Find each parasitized RBC.
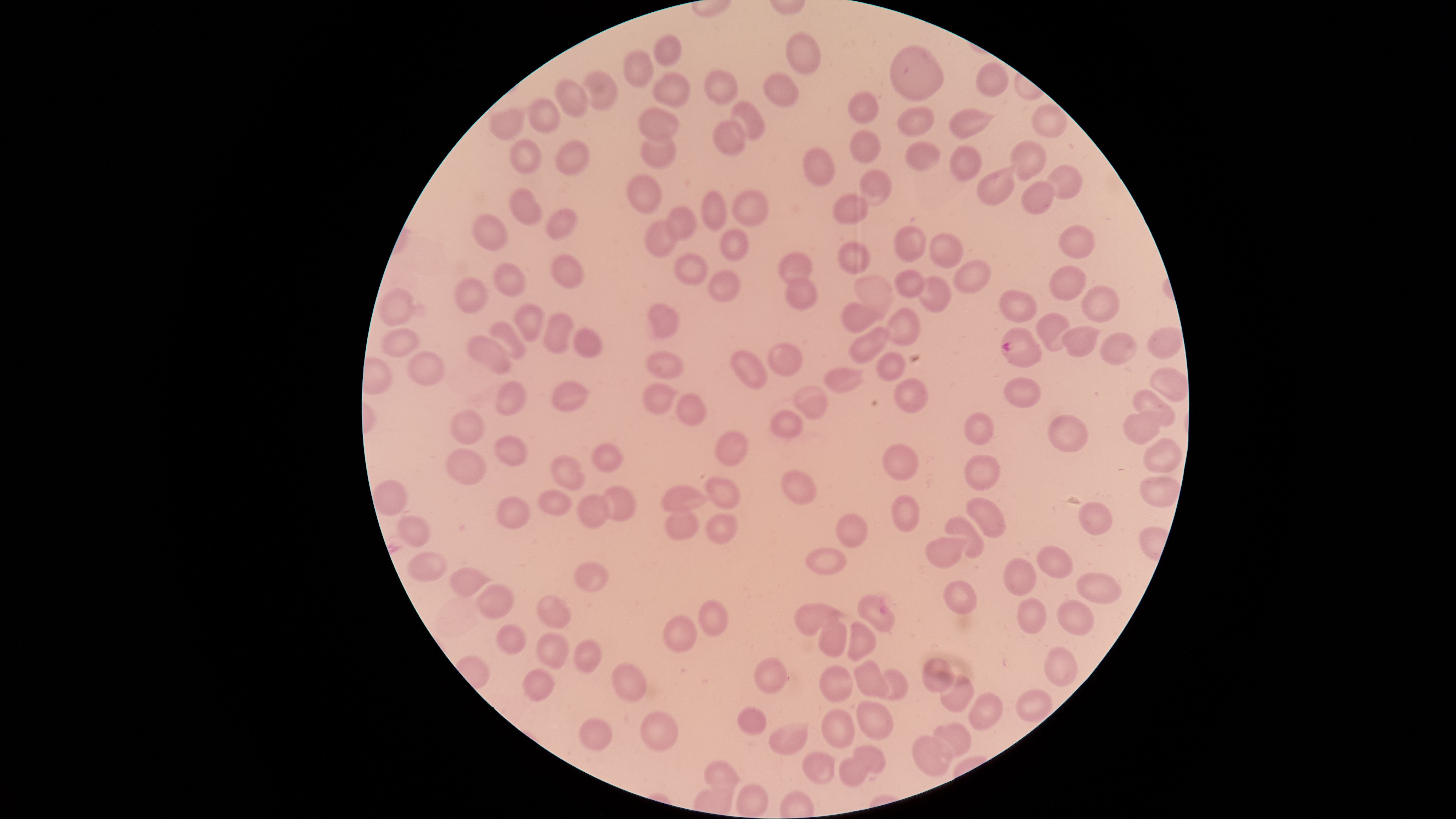

Approximate bounding boxes as (left, top, right, bottom) in pixels.
Parasitized RBCs: (999, 327, 1042, 368).

Approximate bounding boxes as (left, top, right, bottom) in pixels. Uninfected RBCs: (786, 33, 819, 75), (654, 35, 682, 66), (890, 45, 943, 101), (623, 48, 653, 87), (973, 63, 1009, 96), (704, 68, 737, 105), (581, 71, 617, 110), (653, 72, 690, 108), (763, 72, 797, 108), (554, 79, 589, 118), (847, 91, 879, 124), (527, 99, 561, 134), (730, 102, 764, 141), (897, 105, 936, 138), (489, 108, 525, 142), (638, 109, 679, 140), (948, 109, 988, 137), (712, 119, 748, 155), (850, 130, 882, 163), (640, 132, 677, 170), (555, 139, 591, 176), (508, 140, 544, 174), (1009, 140, 1046, 179), (905, 142, 941, 171), (948, 145, 982, 181), (801, 147, 836, 187), (1044, 166, 1083, 199), (859, 169, 894, 207), (975, 169, 1016, 205), (626, 173, 664, 214), (1020, 180, 1057, 215), (509, 187, 543, 226), (733, 190, 769, 226), (703, 192, 727, 230), (831, 194, 869, 225), (666, 206, 697, 239), (545, 210, 580, 240), (472, 213, 509, 253), (644, 219, 678, 258), (1058, 225, 1096, 258), (895, 226, 926, 263), (720, 228, 748, 261), (928, 233, 964, 268), (838, 242, 872, 275), (674, 251, 710, 286), (550, 252, 585, 288), (779, 253, 812, 285), (952, 258, 990, 295), (493, 262, 525, 297), (1049, 264, 1085, 302), (895, 269, 924, 300), (709, 270, 741, 302), (454, 276, 489, 313), (855, 276, 893, 313), (786, 277, 818, 310), (918, 277, 952, 313), (1082, 286, 1118, 323), (377, 289, 417, 325), (999, 290, 1037, 323), (840, 302, 878, 333), (511, 303, 547, 342), (647, 303, 680, 337), (885, 308, 921, 347), (541, 312, 576, 355), (1036, 313, 1073, 351), (489, 321, 527, 360), (1064, 326, 1097, 357), (381, 327, 420, 357), (848, 327, 891, 364), (573, 329, 603, 359), (1101, 333, 1136, 365), (466, 335, 513, 374), (768, 343, 803, 377), (407, 350, 445, 387), (731, 350, 768, 389), (645, 351, 683, 379), (877, 352, 905, 380), (824, 366, 865, 393), (1003, 378, 1041, 408), (496, 379, 527, 415), (894, 380, 929, 412), (551, 382, 587, 411), (643, 383, 673, 415), (794, 385, 828, 419), (1132, 389, 1175, 427), (675, 394, 707, 426), (450, 408, 485, 444), (770, 410, 803, 438), (965, 411, 994, 447), (1122, 413, 1159, 445), (1048, 414, 1088, 453), (716, 429, 750, 467), (493, 436, 527, 465), (1141, 436, 1182, 474), (591, 442, 625, 471), (881, 443, 919, 481), (445, 449, 489, 486), (965, 454, 1000, 490), (551, 455, 586, 489), (781, 469, 816, 505), (704, 475, 741, 508), (1138, 476, 1179, 506), (662, 482, 708, 513), (602, 486, 635, 522), (540, 489, 572, 516), (579, 494, 609, 530), (497, 496, 531, 529), (890, 496, 921, 531), (967, 497, 1006, 538), (1078, 502, 1114, 536), (666, 505, 702, 540), (707, 513, 739, 544), (836, 513, 868, 548), (397, 514, 432, 547), (946, 516, 984, 558), (926, 534, 970, 569), (1037, 545, 1073, 579), (805, 546, 846, 576), (407, 551, 447, 581), (1003, 558, 1037, 597), (576, 562, 609, 592), (451, 567, 492, 598), (1077, 571, 1120, 605), (943, 581, 976, 615), (477, 584, 514, 618), (536, 595, 572, 628), (857, 595, 896, 632), (1017, 597, 1049, 634), (700, 600, 728, 637), (1057, 601, 1093, 636), (795, 603, 839, 635), (664, 615, 697, 654), (816, 617, 850, 659), (839, 622, 875, 660), (497, 624, 526, 654), (537, 631, 569, 667), (574, 638, 602, 673), (1043, 648, 1076, 687), (753, 656, 787, 695), (922, 658, 954, 692), (853, 660, 890, 703), (612, 663, 648, 702), (819, 666, 854, 701), (523, 667, 556, 700), (874, 670, 909, 701), (941, 675, 974, 713), (1016, 689, 1053, 721), (968, 692, 1003, 731), (858, 701, 894, 740), (737, 707, 767, 735), (821, 710, 857, 749), (640, 711, 677, 752), (579, 718, 613, 751), (768, 722, 809, 754), (932, 723, 970, 759), (913, 735, 953, 776), (851, 745, 886, 772), (801, 752, 835, 783), (838, 758, 870, 787), (702, 760, 739, 794). Species: Plasmodium falciparum. Smartphone photograph through the microscope eyepiece. Image is 1456×819 pixels. Giemsa stain. Circular visible region. Single field of view. Thin smear of blood.